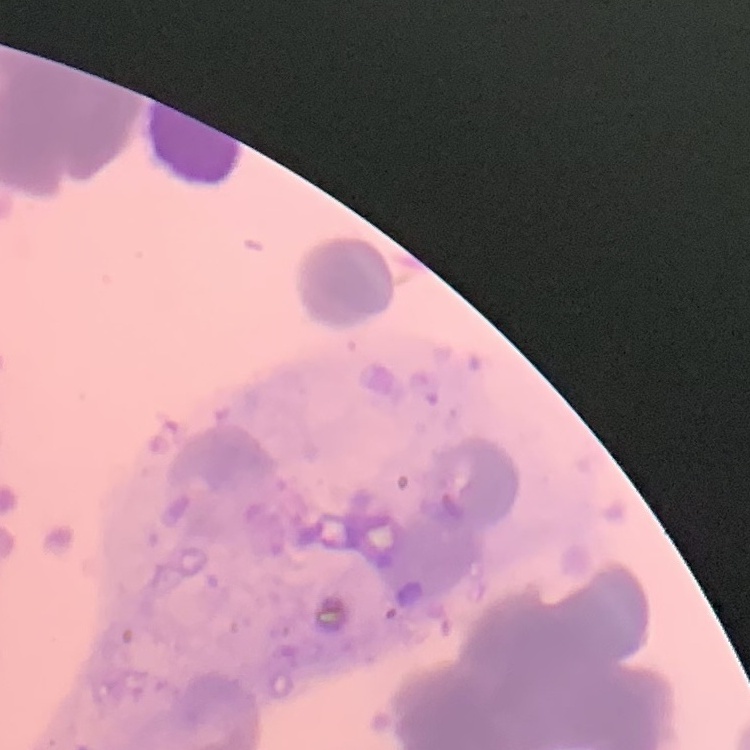

erythrocyte_morphology: rouleaux formation
preparation: thin blood film
stain: Field's or Giemsa
image_type: one tile cut from a larger photomicrograph